Evaluate for malaria.
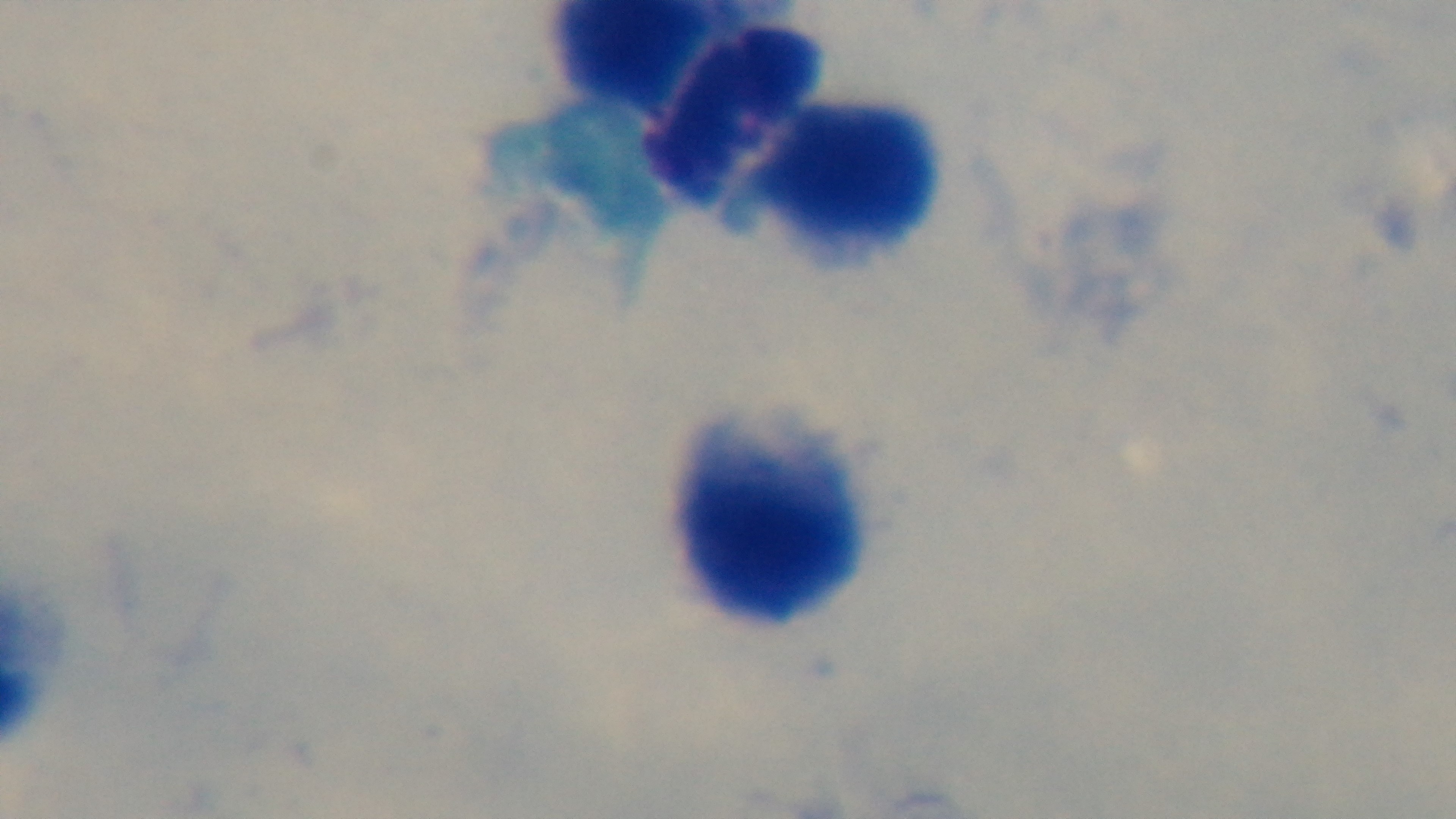
It is uninfected.

Summary:
  - Capture: mounted 4K digital camera
  - Modality: light microscopy
  - Objective: 100x oil immersion
  - Field of view: single
  - Preparation: thick
  - Stain: Giemsa